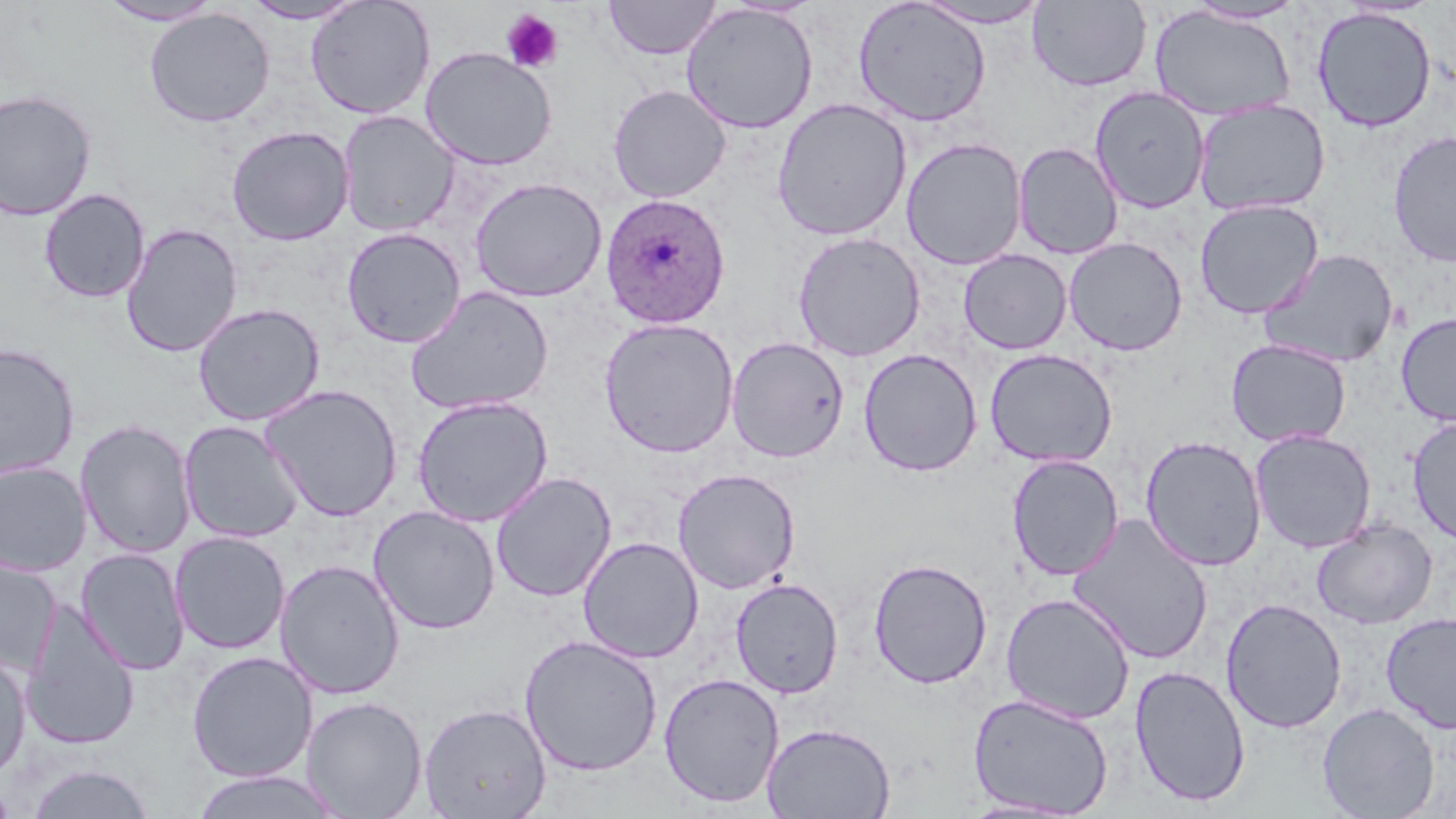

Summary:
  - Coordinate format: approximate bounding boxes as (x1,y1)-(x2,y2) corner pairs in pixels
  - Plasmodium ovale-infected red blood cell locations: (600,192)-(731,328)
  - Uninfected red blood cell locations: (603,0)-(723,60), (97,1)-(225,26), (240,1)-(366,24), (305,1)-(436,120), (853,1)-(991,127), (911,1)-(1055,29), (1028,1)-(1152,92), (1184,1)-(1308,25), (680,3)-(819,134), (1148,5)-(1297,121), (1312,7)-(1437,132), (144,8)-(275,127), (420,46)-(558,170), (607,84)-(731,203), (1089,86)-(1210,213), (0,88)-(98,220), (771,98)-(912,241), (1193,99)-(1331,216), (339,110)-(459,236), (226,125)-(355,245), (1387,130)-(1456,267), (901,137)-(1027,271), (1013,141)-(1123,260), (470,177)-(607,302), (39,188)-(150,303), (1194,198)-(1324,319), (121,223)-(243,358), (341,227)-(466,347), (792,231)-(926,362), (1063,237)-(1188,356), (1259,248)-(1399,369), (958,249)-(1072,355), (405,286)-(554,415), (192,302)-(325,426), (1396,312)-(1456,426), (599,317)-(739,458), (726,335)-(849,463), (1225,338)-(1351,447), (0,342)-(80,481), (858,348)-(983,476), (984,348)-(1118,468), (259,383)-(403,522), (411,395)-(554,527), (1407,416)-(1456,545), (75,418)-(196,559), (179,420)-(305,543), (1249,429)-(1377,553), (1139,435)-(1267,571), (1006,454)-(1124,581), (0,461)-(92,577), (672,468)-(800,594), (491,471)-(617,602), (367,505)-(501,634), (1067,514)-(1214,665), (1311,518)-(1437,629), (169,531)-(291,654), (577,536)-(704,664), (75,547)-(190,675), (0,553)-(61,674), (868,557)-(993,689), (275,559)-(405,699), (730,577)-(843,698), (1000,592)-(1135,724), (1221,597)-(1347,734), (22,599)-(141,751), (1380,611)-(1456,734), (519,633)-(663,776), (0,649)-(31,780), (186,651)-(318,782), (1129,664)-(1251,807), (658,672)-(785,808), (967,693)-(1115,816), (300,695)-(428,818), (419,702)-(552,818), (1316,702)-(1440,818), (761,721)-(896,819), (25,763)-(156,819), (191,769)-(343,818)
  - Platelet locations: (500,9)-(563,73)
  - Slide-level diagnosis: Plasmodium ovale
  - Stain: May-Grünwald-Giemsa
  - Image size: 1456×819 pixels
  - Field of view: one of a larger specimen
  - Magnification: 1000x
  - Preparation: thin blood film
  - Modality: optical microscopy